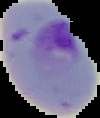
Summary:
  - Malaria status: parasitized
  - Image size: 100×118 pixels
  - Image type: cell region segmented out of the field of view; surrounding area masked to black
  - Preparation: thin blood smear